Assess this cell for malaria.
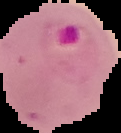
It is parasitized.

Summary:
  - Image size: 121×133 pixels
  - Preparation: thin blood smear
  - Image type: segmented cell region with the area outside set to black